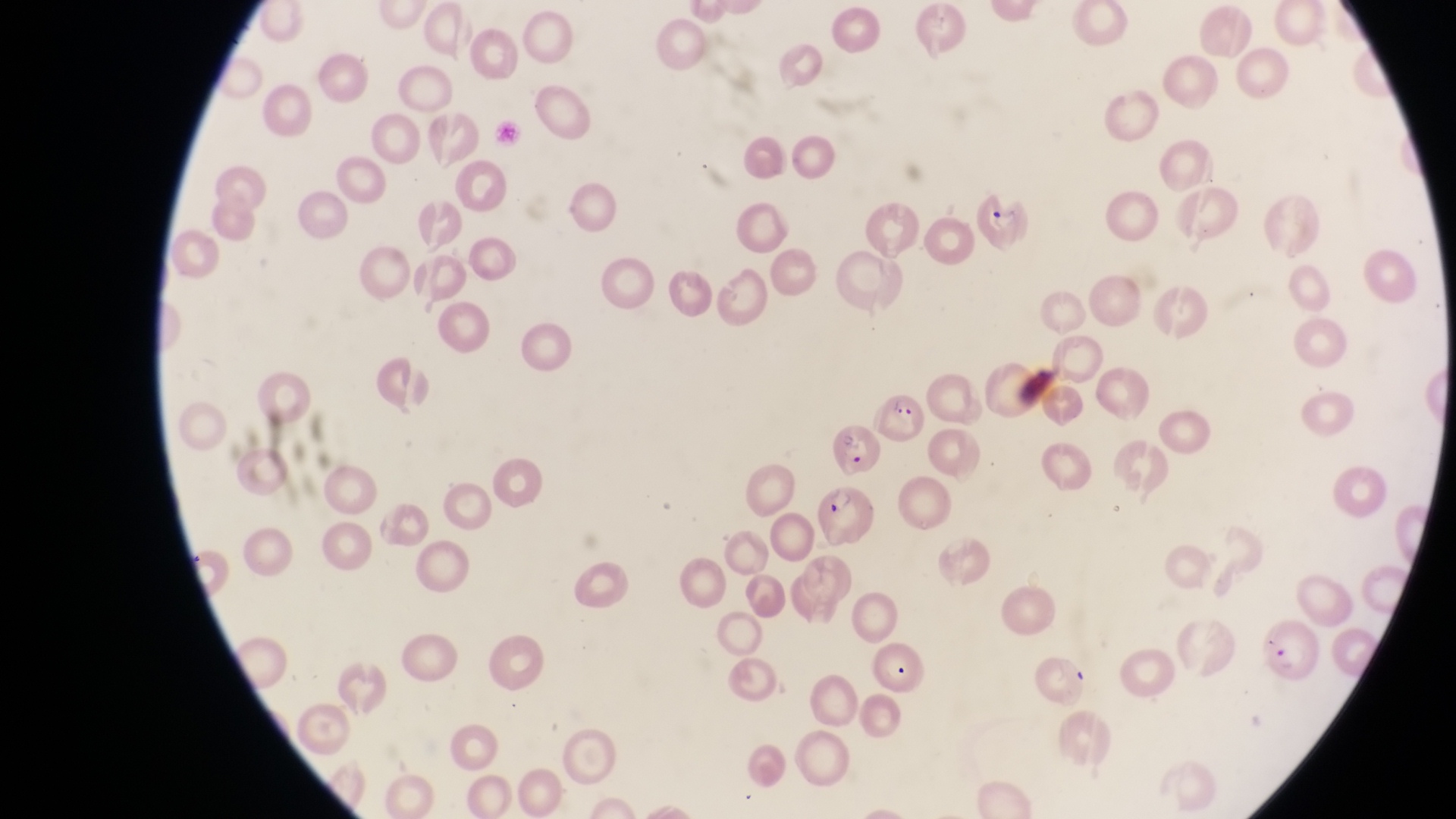
preparation = thin blood smear
parasitised red blood cell locations = approximate bounding boxes as {left, top, right, bottom} in pixels: {974, 185, 1030, 251}, {869, 386, 922, 442}, {819, 482, 875, 542}, {1265, 620, 1318, 681}
country = Uganda
image size = 1456×819 pixels
field of view = single
capture = smartphone photograph through the eyepiece of an Olympus CX-23 microscope
magnification = 1000x